Assess the morphology of the erythrocytes.
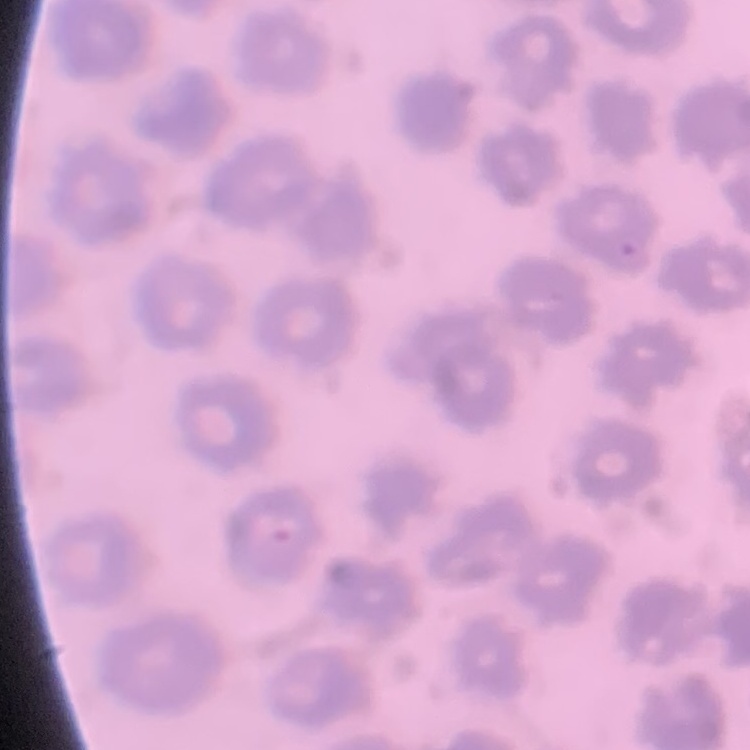

No rouleaux formation.

One tile cut from a larger photomicrograph. Thin peripheral smear. Field's or Giemsa stain.